Give the position of every Plasmodium parasite.
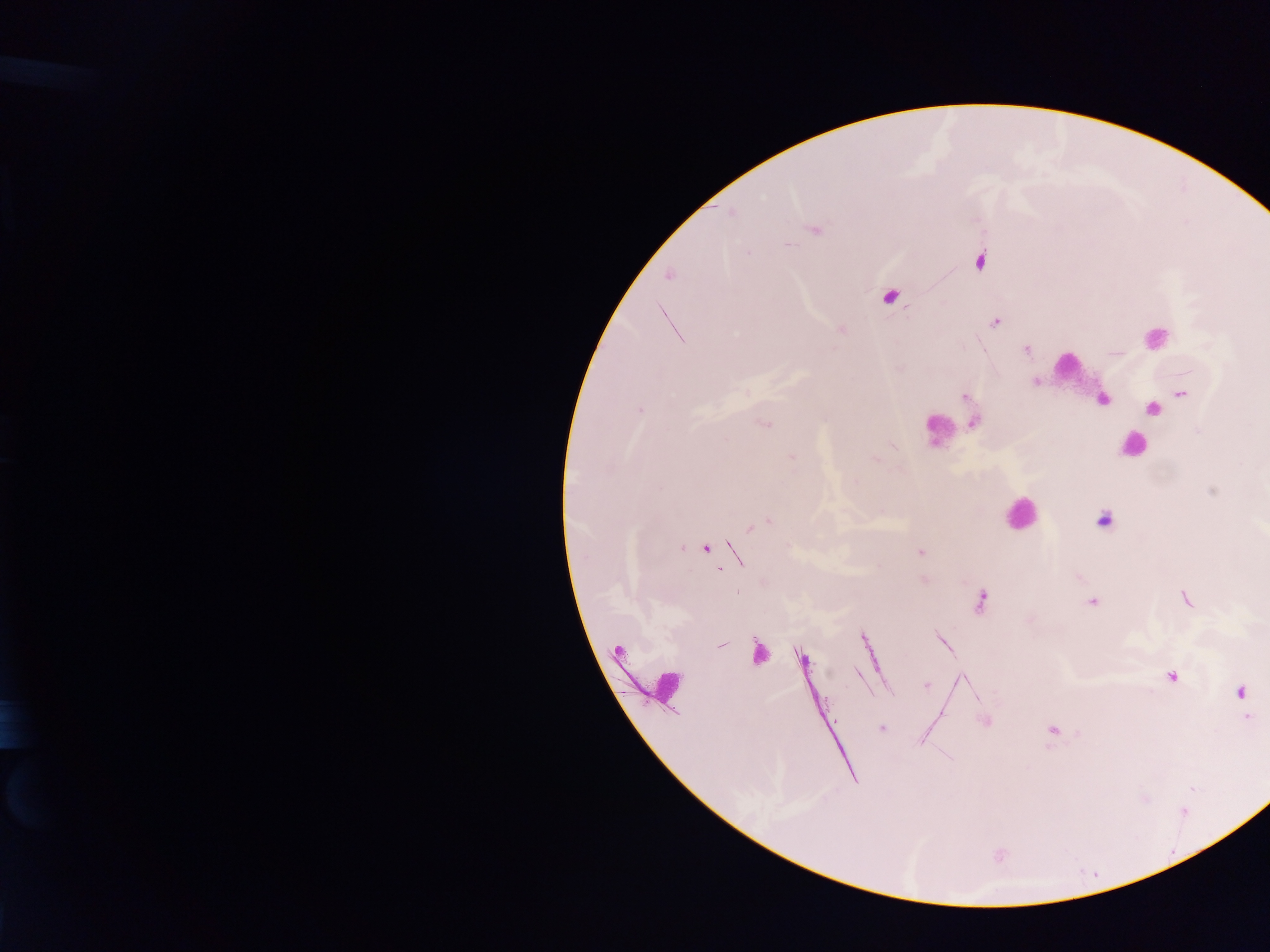

Approximate centers as [x, y] in pixels.
Plasmodium parasites: [731, 213], [815, 229], [788, 245], [979, 260], [668, 276], [889, 297], [995, 322], [1026, 349], [1035, 381], [1182, 394], [965, 397], [641, 410], [1152, 410], [973, 423], [765, 424], [791, 458], [876, 459], [1103, 521], [766, 523], [751, 527], [682, 547], [705, 549], [919, 553], [924, 579], [1185, 599], [981, 600], [1093, 602], [722, 644], [801, 658], [1171, 676], [927, 684], [1240, 691], [1248, 717], [985, 721], [881, 728], [1053, 731].

{
  "preparation": "thick blood smear",
  "field_of_view": "single",
  "leukocyte_locations": "approximate centers as [x, y] in pixels: [1155, 337], [1067, 365], [1103, 403], [944, 429], [1132, 444], [1019, 514], [754, 651], [662, 690]",
  "capture": "mobile-phone photograph through a microscope",
  "image_size": "1270×952 pixels",
  "country": "Ghana"
}